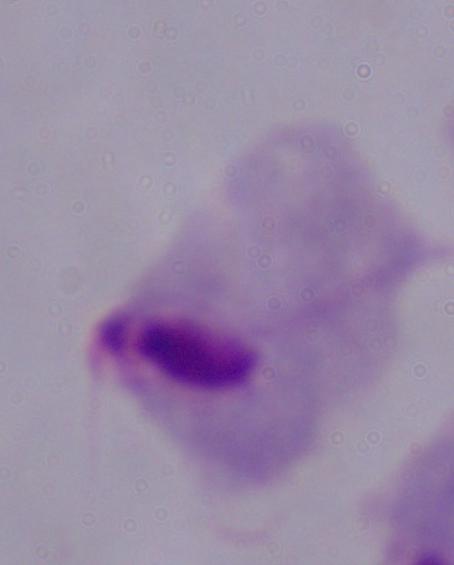
magnification: 1000x
modality: photomicrograph
identification: trichomonad